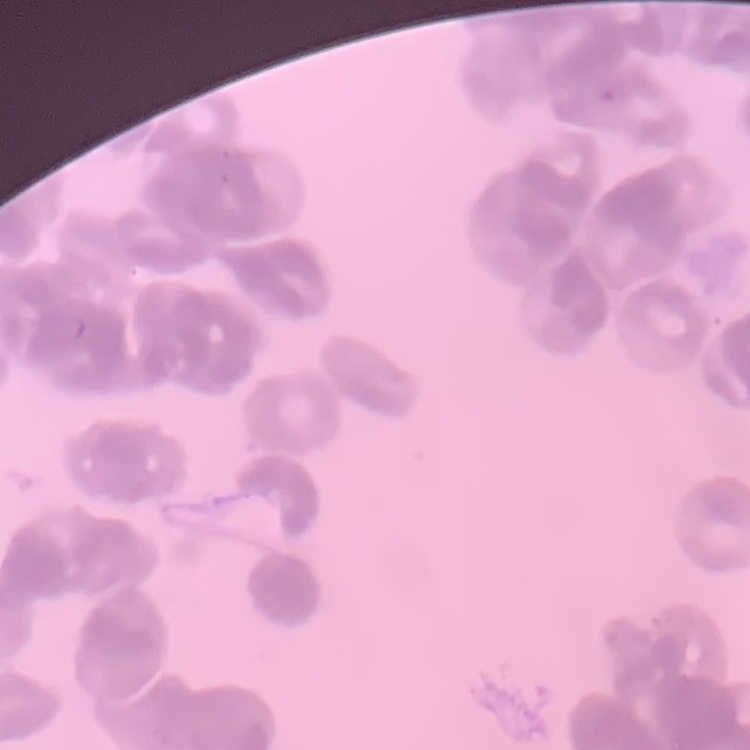
The red blood cells exhibit rouleaux formation. Stained with either Field's or Giemsa. One tile cut from a larger photomicrograph. Thin blood smear.